Assess the morphology of the red blood cells.
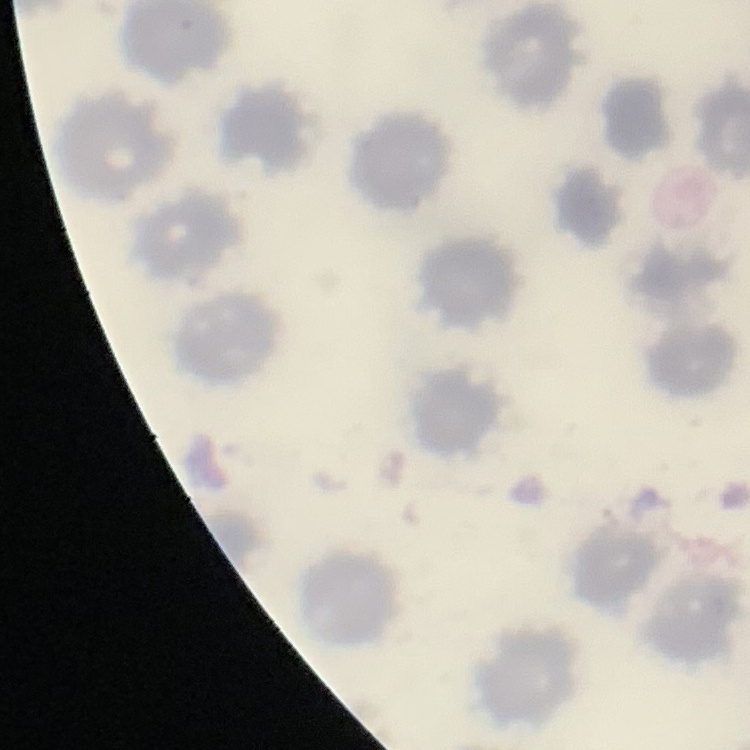

No rouleaux formation.

Summary:
  - Image type: square crop of a larger photomicrograph
  - Preparation: thin blood smear
  - Stain: Field's or Giemsa